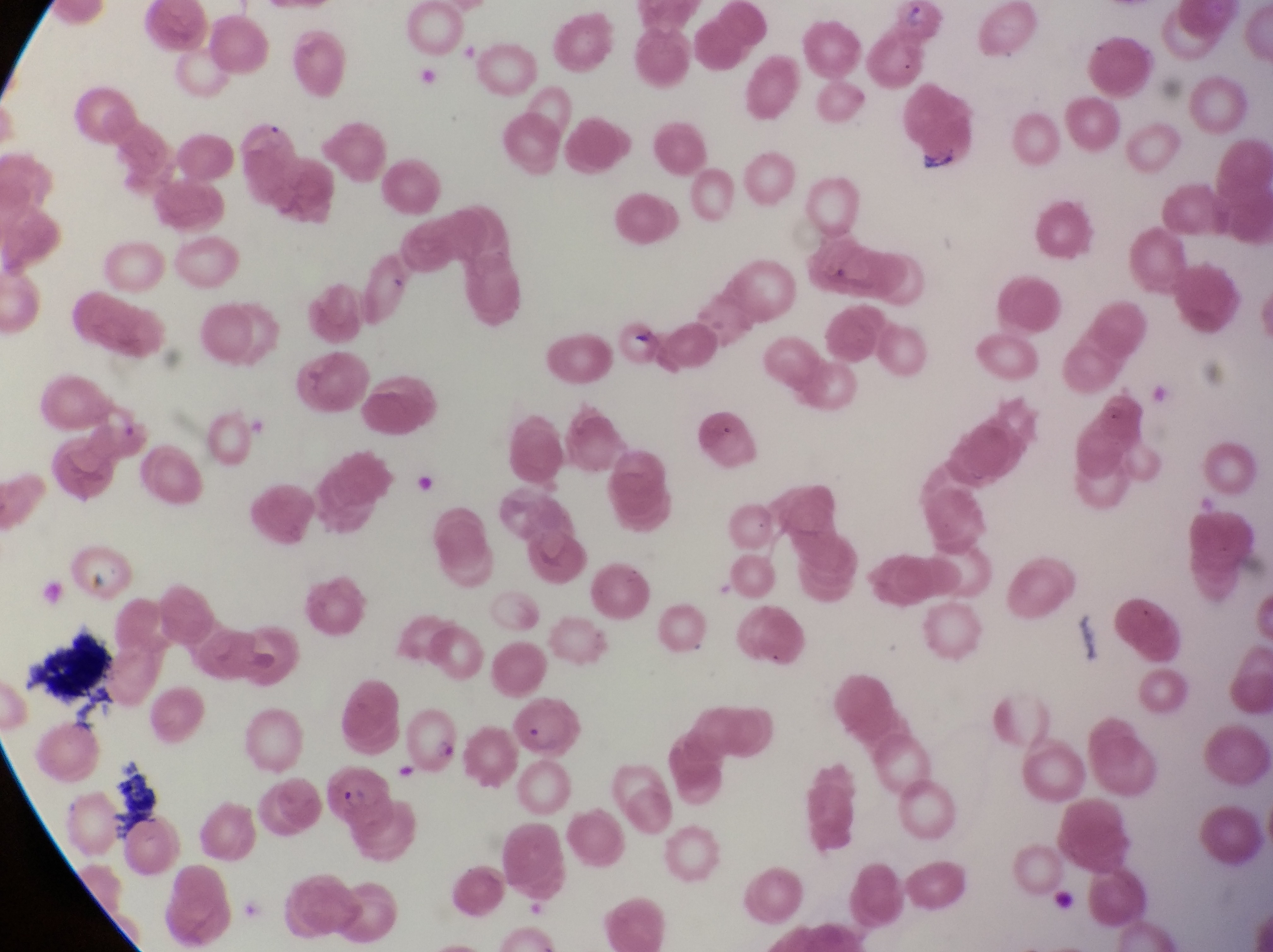

Approximate bounding boxes as left top right bottom in pixels. Artifact (platelet-like body, stain precipitate, or debris) locations: 29 633 126 722; 107 760 160 839. Parasitised red blood cell locations: 229 112 304 205; 507 702 589 759; 400 705 469 782; 324 761 389 824. Sample from Uganda. Thin blood smear. Single field of view. Captured by a smartphone held over the eyepiece of an Olympus CX-23 microscope. Image is 1273×952 pixels. At a magnification of 1000x.